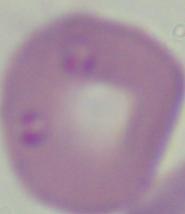 Micrograph. Captured at 1000x magnification. A Babesia parasite is seen.